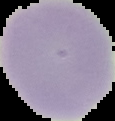
Summary:
  - Image type: cell region segmented out of the field of view; surrounding area masked to black
  - Preparation: thin blood smear
  - Result: negative for Plasmodium parasites
  - Image size: 115×121 pixels